Describe the morphology of the red blood cells.
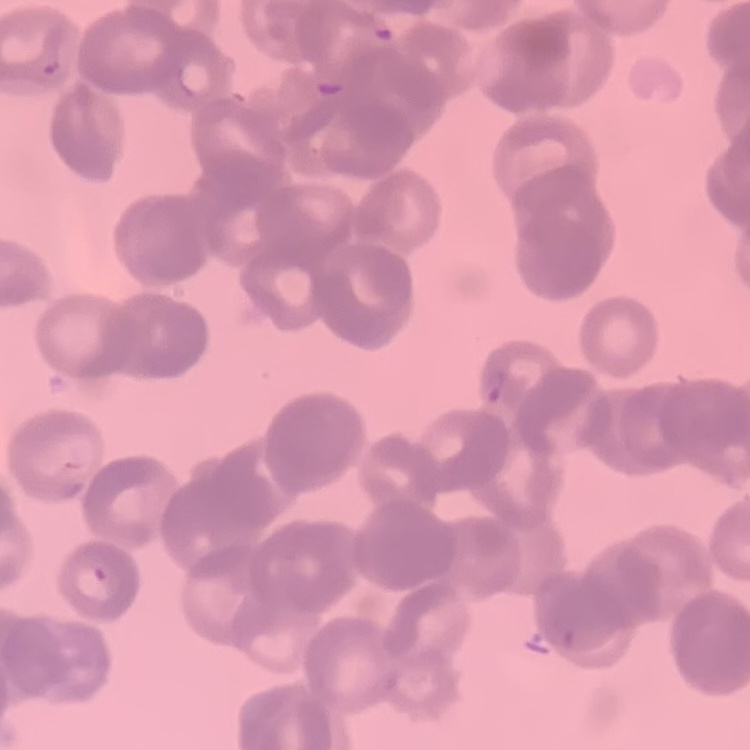

Rouleaux formation.

Summary:
  - Image type: one tile cut from a larger photomicrograph
  - Preparation: thin blood smear
  - Stain: Field's or Giemsa